Report the malaria status of this cell.
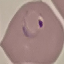

Parasitized.

capture = smartphone through the microscope eyepiece
image type = cell patch, automatically extracted from a larger field of view and resized to 64 × 64 pixels
preparation = thin blood smear
stain = Giemsa